Give the extent of all Plasmodium malariae-infected red blood cells.
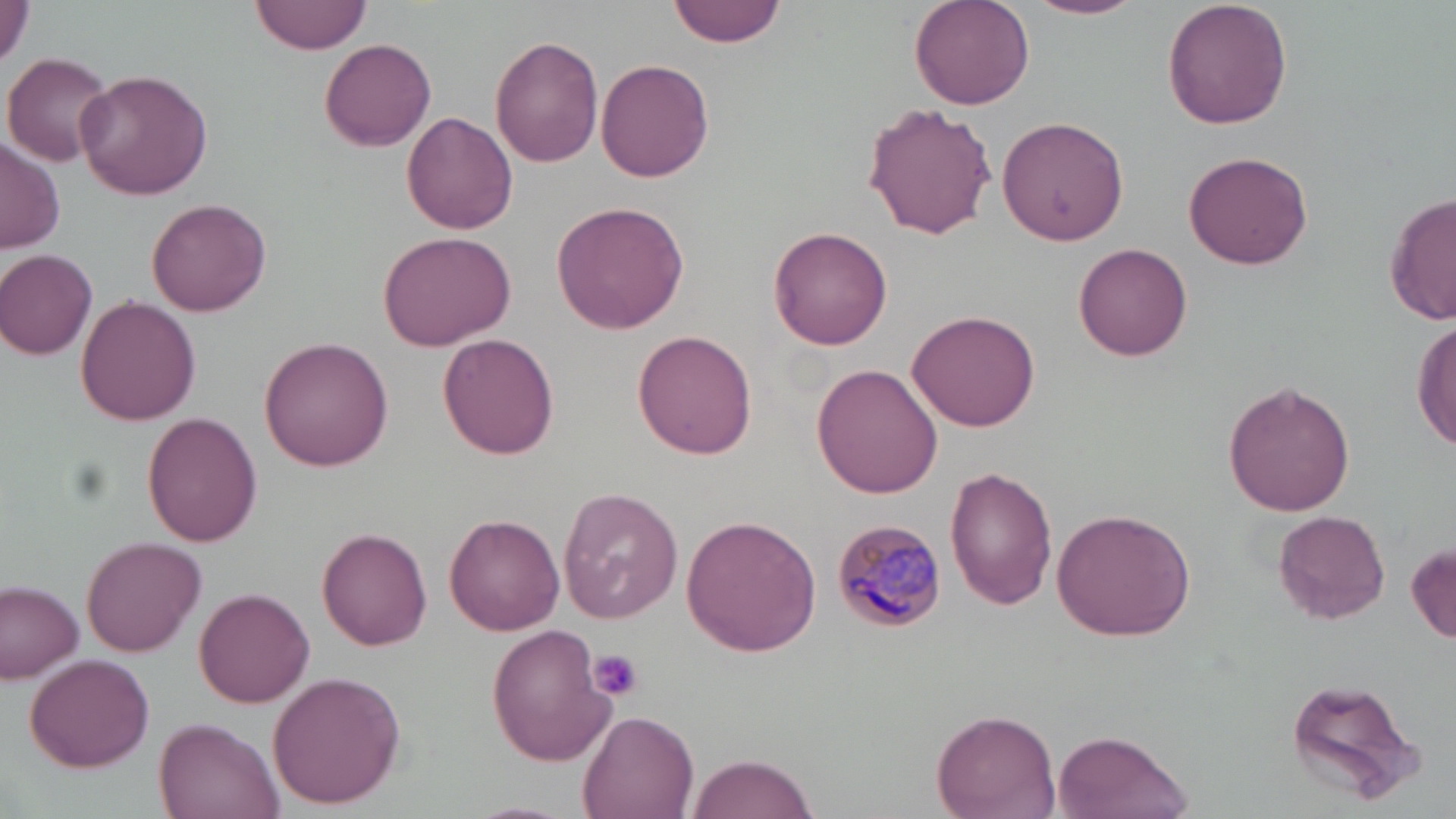
Approximate bounding boxes as [x1, y1, x2, y2] in pixels.
Plasmodium malariae-infected red blood cells: [831, 520, 948, 632].

Summary:
  - Platelet locations: [585, 650, 644, 702]
  - Uninfected red blood cell locations: [0, 0, 30, 72], [250, 0, 370, 56], [668, 0, 788, 47], [1026, 0, 1145, 21], [1162, 0, 1292, 130], [909, 1, 1036, 110], [490, 35, 605, 169], [319, 37, 436, 151], [2, 51, 115, 167], [596, 57, 715, 183], [76, 67, 213, 200], [863, 102, 998, 241], [402, 112, 518, 235], [996, 115, 1131, 248], [0, 140, 64, 253], [1183, 149, 1315, 270], [1384, 192, 1455, 327], [146, 198, 270, 315], [550, 200, 691, 334], [768, 226, 893, 351], [379, 231, 514, 350], [1073, 242, 1193, 362], [0, 248, 99, 360], [75, 296, 200, 425], [906, 306, 1042, 431], [1413, 316, 1455, 456], [633, 331, 758, 460], [437, 334, 559, 460], [258, 336, 394, 471], [812, 363, 944, 499], [1222, 380, 1355, 517], [143, 414, 262, 546], [946, 466, 1058, 610], [556, 489, 682, 623], [1049, 509, 1198, 642], [1273, 511, 1390, 623], [444, 514, 564, 636], [681, 514, 823, 656], [317, 525, 433, 649], [81, 537, 205, 656], [1407, 541, 1456, 645], [0, 581, 84, 683], [194, 589, 315, 707], [488, 625, 616, 765], [23, 651, 154, 770], [266, 670, 407, 809], [1282, 675, 1424, 807], [931, 707, 1061, 818], [577, 708, 702, 818], [152, 718, 284, 818], [1051, 729, 1195, 819], [685, 752, 818, 819]
  - Slide-level diagnosis: Plasmodium malariae
  - Field of view: single
  - Image size: 1456×819 pixels
  - Magnification: 1000x
  - Preparation: thin blood smear
  - Modality: optical microscopy
  - Stain: May-Grünwald-Giemsa